Comment on the morphology of the red blood cells.
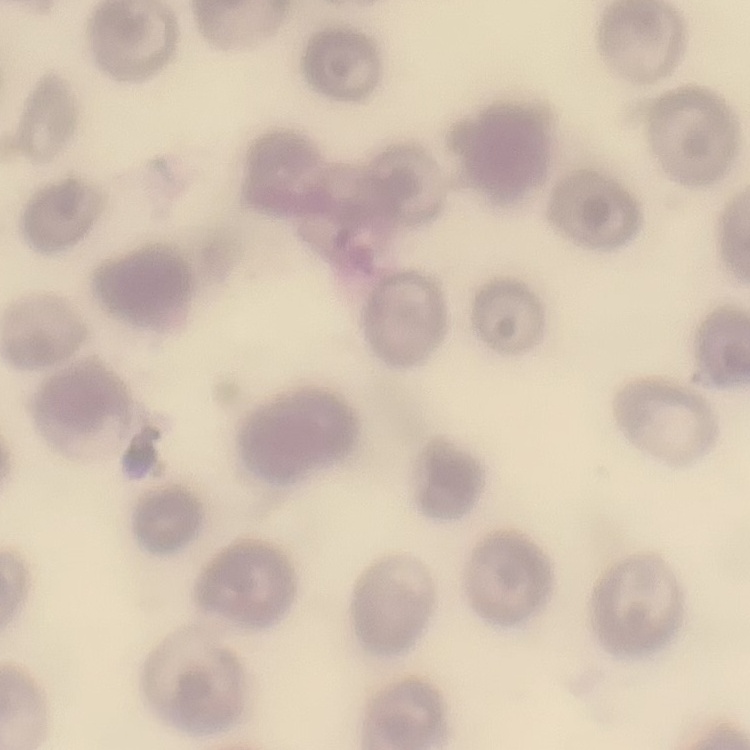

They show no rouleaux formation.

Thin peripheral smear. One tile cut from a larger photomicrograph. Field's or Giemsa stain.